Name the parasite shown.
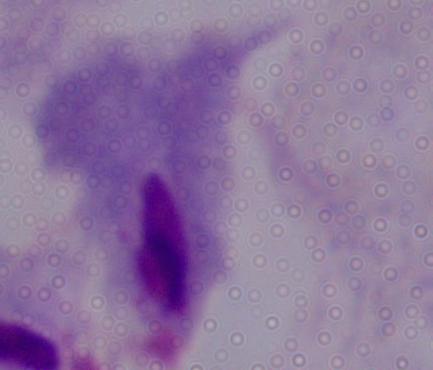

This is a trichomonad.

magnification = 1000x
modality = photomicrograph